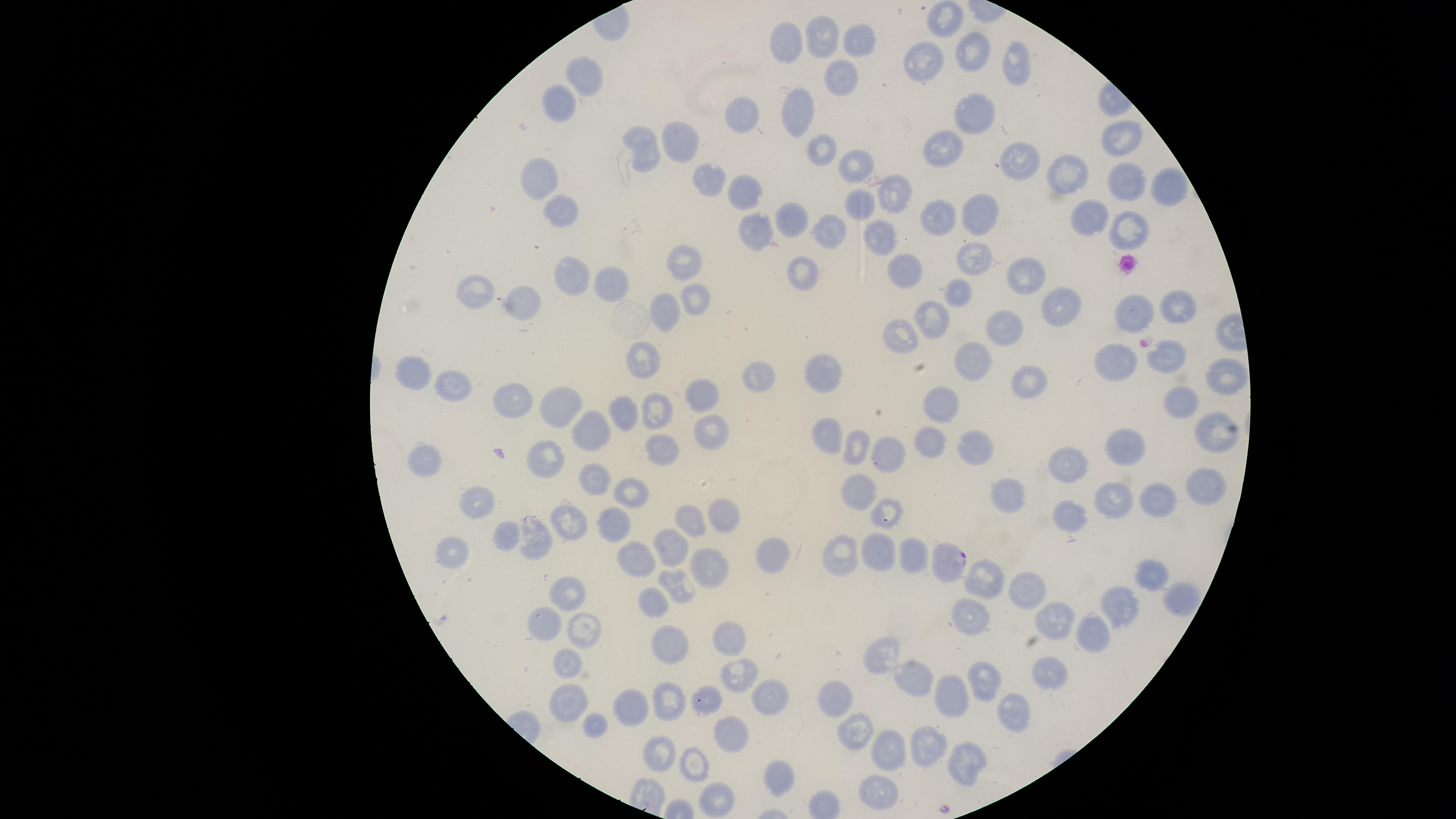
preparation: thin blood film
presence: malaria parasites detected
stain: Giemsa
field_of_view: single
image_size: 1456×819 pixels
uninfected_red_blood_cells: 'approximate marker points, in pixels from the top-left corner: (x=942, y=16), (x=859, y=39), (x=826, y=40), (x=792, y=43), (x=968, y=53), (x=922, y=62), (x=1014, y=64), (x=589, y=70), (x=837, y=80), (x=563, y=99), (x=799, y=110), (x=973, y=111), (x=742, y=117), (x=1120, y=139), (x=677, y=141), (x=645, y=145), (x=826, y=148), (x=943, y=151), (x=852, y=159), (x=1014, y=164), (x=1060, y=171), (x=540, y=173), (x=708, y=179), (x=1121, y=183), (x=1169, y=187), (x=743, y=191), (x=892, y=195), (x=563, y=207), (x=859, y=207), (x=935, y=214), (x=976, y=214), (x=1091, y=217), (x=795, y=219), (x=1128, y=227), (x=760, y=230), (x=877, y=232), (x=824, y=233), (x=978, y=259), (x=684, y=262), (x=904, y=270), (x=804, y=271), (x=1023, y=273), (x=572, y=279), (x=604, y=280), (x=956, y=288), (x=480, y=291), (x=694, y=297), (x=1061, y=301), (x=1175, y=303), (x=522, y=304), (x=660, y=309), (x=1133, y=309), (x=930, y=311), (x=1003, y=325), (x=904, y=331), (x=1169, y=354), (x=972, y=358), (x=640, y=361), (x=1114, y=361), (x=413, y=371), (x=826, y=372), (x=1225, y=374), (x=1020, y=380), (x=754, y=382), (x=451, y=388), (x=513, y=396), (x=698, y=396), (x=1185, y=399), (x=942, y=400), (x=557, y=401), (x=630, y=410), (x=653, y=412), (x=589, y=423), (x=708, y=434), (x=825, y=434), (x=1214, y=436), (x=926, y=444), (x=853, y=446), (x=1119, y=446), (x=973, y=450), (x=663, y=453), (x=882, y=455), (x=543, y=457), (x=427, y=464), (x=1072, y=464), (x=595, y=479), (x=1206, y=484), (x=855, y=490), (x=631, y=494), (x=1014, y=494), (x=1154, y=498), (x=1116, y=500), (x=482, y=508), (x=725, y=512), (x=888, y=512), (x=1071, y=518), (x=696, y=522), (x=568, y=523), (x=610, y=523), (x=542, y=536), (x=676, y=541), (x=509, y=542), (x=912, y=549), (x=768, y=551), (x=878, y=553), (x=444, y=559), (x=639, y=559), (x=841, y=561), (x=712, y=567), (x=1149, y=570), (x=987, y=580), (x=673, y=581), (x=1032, y=589), (x=1176, y=591), (x=565, y=595), (x=650, y=600), (x=1121, y=607), (x=969, y=611), (x=1056, y=622), (x=543, y=623), (x=587, y=631), (x=1091, y=634), (x=726, y=636), (x=671, y=643), (x=888, y=655), (x=570, y=666), (x=1050, y=672), (x=744, y=673), (x=912, y=674), (x=985, y=675), (x=763, y=691), (x=671, y=697), (x=714, y=697), (x=949, y=697), (x=837, y=699), (x=573, y=708), (x=626, y=709), (x=1010, y=710), (x=598, y=727), (x=852, y=728), (x=738, y=730), (x=661, y=747), (x=924, y=747), (x=883, y=751), (x=964, y=760), (x=696, y=765), (x=779, y=775), (x=878, y=792), (x=719, y=797)'
visible_region: circular
capture: smartphone photograph through the microscope eyepiece
species: Plasmodium falciparum
parasitized_red_blood_cells: 'approximate marker points, in pixels from the top-left corner: (x=945, y=558)'